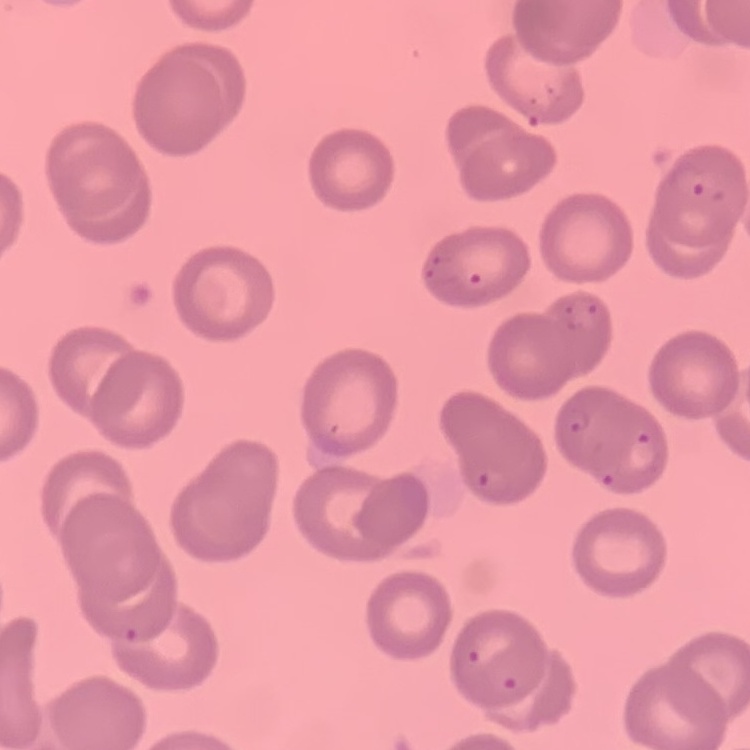
Summary:
  - Red blood cell morphology: no rouleaux formation
  - Stain: Field's or Giemsa
  - Preparation: thin peripheral smear
  - Image type: square crop of a larger photomicrograph